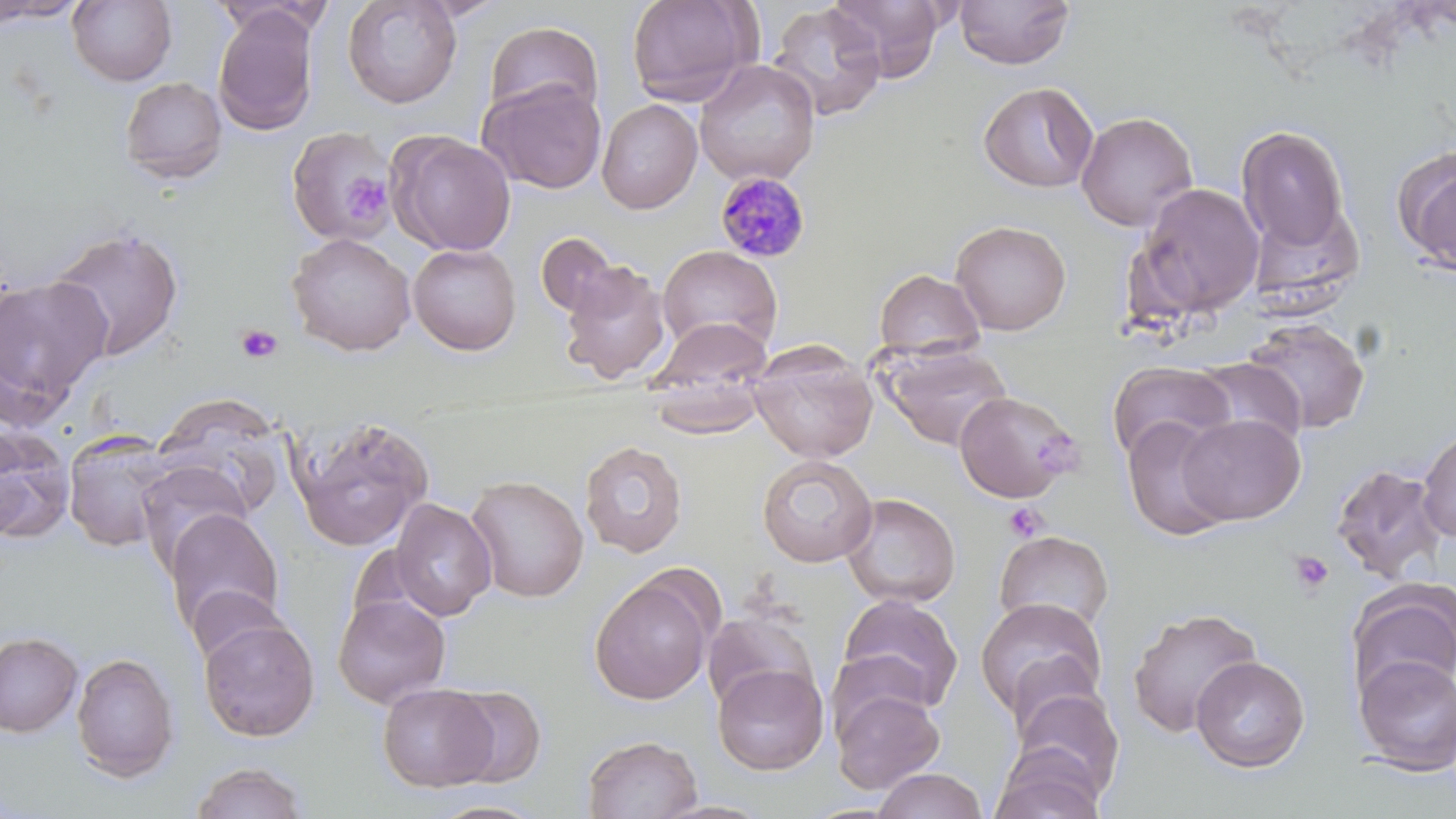
{
  "slide_level_diagnosis": "Plasmodium malariae",
  "image_size": "1456×819 pixels",
  "platelet_locations": "approximate bounding boxes as (x1, y1, x2, y2) in pixels: (342, 174, 390, 222), (236, 323, 282, 364), (1004, 501, 1049, 542), (1288, 549, 1335, 598)",
  "preparation": "thin blood smear",
  "field_of_view": "one of a larger specimen",
  "modality": "light microscopy",
  "plasmodium_malariae_infected_red_blood_cell_locations": "approximate bounding boxes as (x1, y1, x2, y2) in pixels: (714, 172, 811, 263)",
  "magnification": "1000x",
  "uninfected_red_blood_cell_locations": "approximate bounding boxes as (x1, y1, x2, y2) in pixels: (0, 0, 84, 22), (67, 0, 177, 86), (342, 0, 463, 109), (409, 0, 511, 22), (625, 0, 760, 106), (827, 0, 948, 81), (953, 0, 1076, 70), (212, 1, 335, 38), (766, 3, 887, 122), (213, 7, 319, 136), (483, 21, 604, 123), (694, 59, 820, 185), (120, 76, 227, 184), (478, 78, 608, 195), (977, 81, 1098, 193), (597, 98, 703, 214), (1076, 112, 1199, 232), (1236, 125, 1351, 253), (285, 127, 391, 247), (387, 131, 517, 256), (1392, 144, 1456, 275), (1134, 182, 1265, 320), (1246, 201, 1363, 310), (950, 220, 1072, 335), (45, 226, 185, 363), (536, 232, 626, 323), (286, 233, 416, 356), (408, 243, 522, 355), (658, 245, 782, 356), (558, 261, 672, 385), (873, 268, 986, 361), (0, 274, 111, 421), (647, 316, 773, 406), (1241, 317, 1371, 434), (748, 339, 878, 463), (878, 342, 1013, 451), (1192, 357, 1307, 451), (1107, 360, 1237, 464), (645, 369, 771, 440), (955, 390, 1081, 503), (149, 395, 289, 518), (1177, 413, 1306, 525), (291, 416, 435, 551), (1121, 416, 1235, 542), (0, 424, 75, 545), (1417, 427, 1456, 545), (62, 430, 178, 553), (579, 440, 688, 558), (756, 454, 878, 568), (136, 459, 253, 572), (1330, 463, 1448, 585), (465, 474, 589, 602), (840, 492, 961, 608), (390, 498, 497, 620), (163, 508, 285, 637), (993, 530, 1114, 634), (589, 575, 715, 706), (1348, 580, 1456, 701), (187, 585, 291, 668), (836, 592, 964, 716), (333, 594, 451, 708), (974, 597, 1108, 725), (1126, 606, 1264, 738), (702, 609, 820, 714), (198, 616, 320, 742), (0, 632, 83, 737), (71, 652, 180, 782), (1352, 653, 1456, 775), (1191, 657, 1309, 773), (712, 663, 829, 775), (378, 682, 499, 793), (831, 683, 945, 794), (440, 684, 547, 788), (1012, 685, 1125, 804), (582, 734, 703, 819), (989, 749, 1108, 819), (189, 761, 309, 818), (871, 768, 989, 819), (426, 798, 550, 819)",
  "stain": "May-Grünwald-Giemsa"
}